Locate every blood parasite and identify its species.
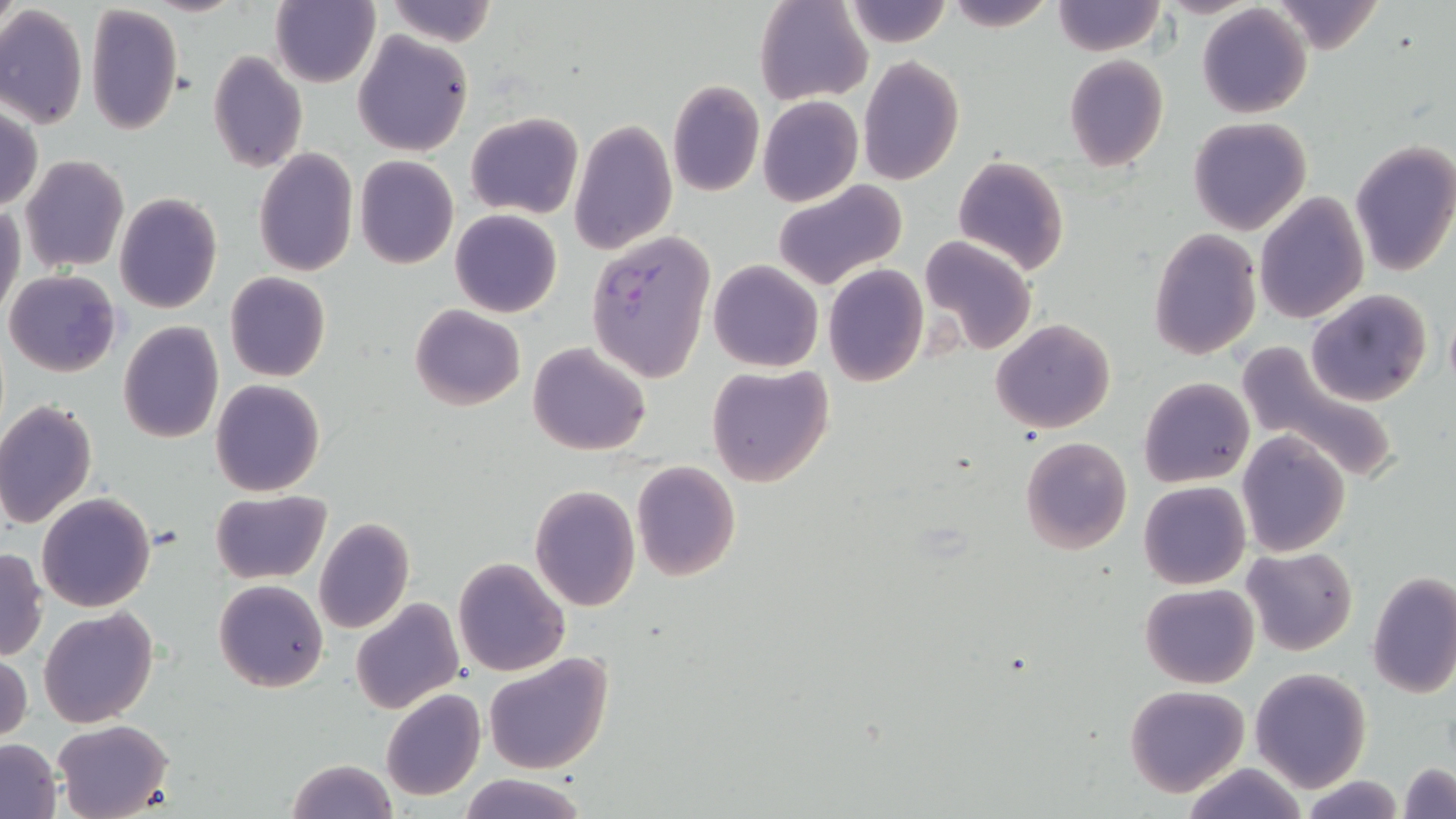

Approximate bounding boxes as (x1, y1, x2, y2) in pixels.
Plasmodium falciparum-infected red blood cells: (586, 231, 714, 383).
No Plasmodium ovale, Plasmodium malariae, Plasmodium vivax, Babesia divergens, or Trypanosoma brucei observed.

slide-level diagnosis = Plasmodium falciparum
image size = 1456×819 pixels
preparation = thin blood film
uninfected red blood cell locations = approximate bounding boxes as (x1, y1, x2, y2) in pixels: (270, 0, 379, 87), (383, 0, 498, 47), (755, 0, 871, 105), (942, 0, 1056, 30), (1051, 0, 1165, 55), (1266, 0, 1387, 54), (841, 1, 952, 49), (84, 3, 184, 136), (1198, 4, 1312, 119), (0, 7, 87, 130), (353, 32, 473, 157), (207, 50, 308, 173), (1063, 55, 1168, 171), (858, 56, 964, 186), (666, 80, 764, 198), (757, 96, 862, 207), (1, 106, 42, 212), (465, 111, 583, 220), (1187, 118, 1312, 236), (569, 119, 677, 255), (1349, 142, 1456, 277), (252, 148, 358, 278), (20, 154, 130, 274), (953, 155, 1069, 276), (354, 156, 459, 269), (773, 179, 909, 292), (1255, 190, 1368, 324), (115, 192, 222, 313), (0, 201, 24, 323), (450, 209, 562, 318), (1150, 227, 1261, 360), (919, 233, 1038, 356), (708, 260, 823, 372), (824, 263, 929, 386), (5, 270, 121, 377), (224, 271, 331, 383), (1305, 289, 1432, 406), (410, 304, 526, 411), (990, 318, 1116, 433), (118, 321, 223, 442), (527, 341, 653, 456), (1236, 343, 1402, 485), (707, 364, 834, 487), (1139, 377, 1254, 488), (211, 379, 325, 496), (0, 399, 98, 532), (1237, 429, 1352, 556), (1020, 436, 1133, 556), (630, 461, 742, 583), (1138, 480, 1251, 590), (530, 483, 641, 612), (211, 490, 330, 585), (37, 492, 156, 612), (313, 517, 415, 634), (1241, 547, 1358, 655), (0, 549, 47, 661), (454, 557, 569, 677), (1367, 572, 1456, 698), (214, 579, 327, 692), (1139, 582, 1259, 688), (350, 598, 464, 714), (39, 607, 159, 729), (1, 649, 32, 745), (483, 651, 614, 776), (1249, 667, 1372, 792), (1124, 684, 1249, 797), (379, 688, 485, 801), (54, 719, 173, 819), (0, 738, 62, 817), (284, 758, 397, 819), (1179, 762, 1312, 819), (1399, 762, 1455, 818), (459, 773, 586, 819), (1300, 776, 1405, 818)
magnification = 1000x
stain = May-Grünwald-Giemsa
modality = optical microscopy
field of view = one of a larger specimen